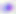

Micrograph. Captured at 400x magnification. Toxoplasma gondii is seen.